Name the cell type shown.
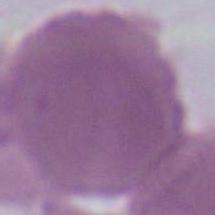

An erythrocyte.

Summary:
  - Magnification: 1000x
  - Modality: photomicrograph